Classify this cell by malaria status.
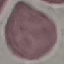

Uninfected.

image type = automatically extracted cell patch, resized to 64 × 64 pixels
preparation = thin smear
capture = smartphone camera at the microscope eyepiece
stain = Giemsa